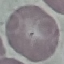
Summary:
  - Malaria status: uninfected
  - Stain: Giemsa
  - Preparation: thin smear
  - Image type: automatically extracted cell patch, resized to 64 × 64 pixels
  - Capture: smartphone through the microscope eyepiece